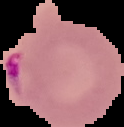

image_size: 124×127 pixels
preparation: thin blood smear
image_type: segmented cell region on a black background
result: malaria parasites detected